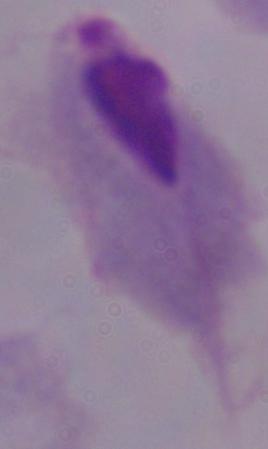 A trichomonad is shown. Photomicrograph. Captured at 1000x magnification.